Outline platelets.
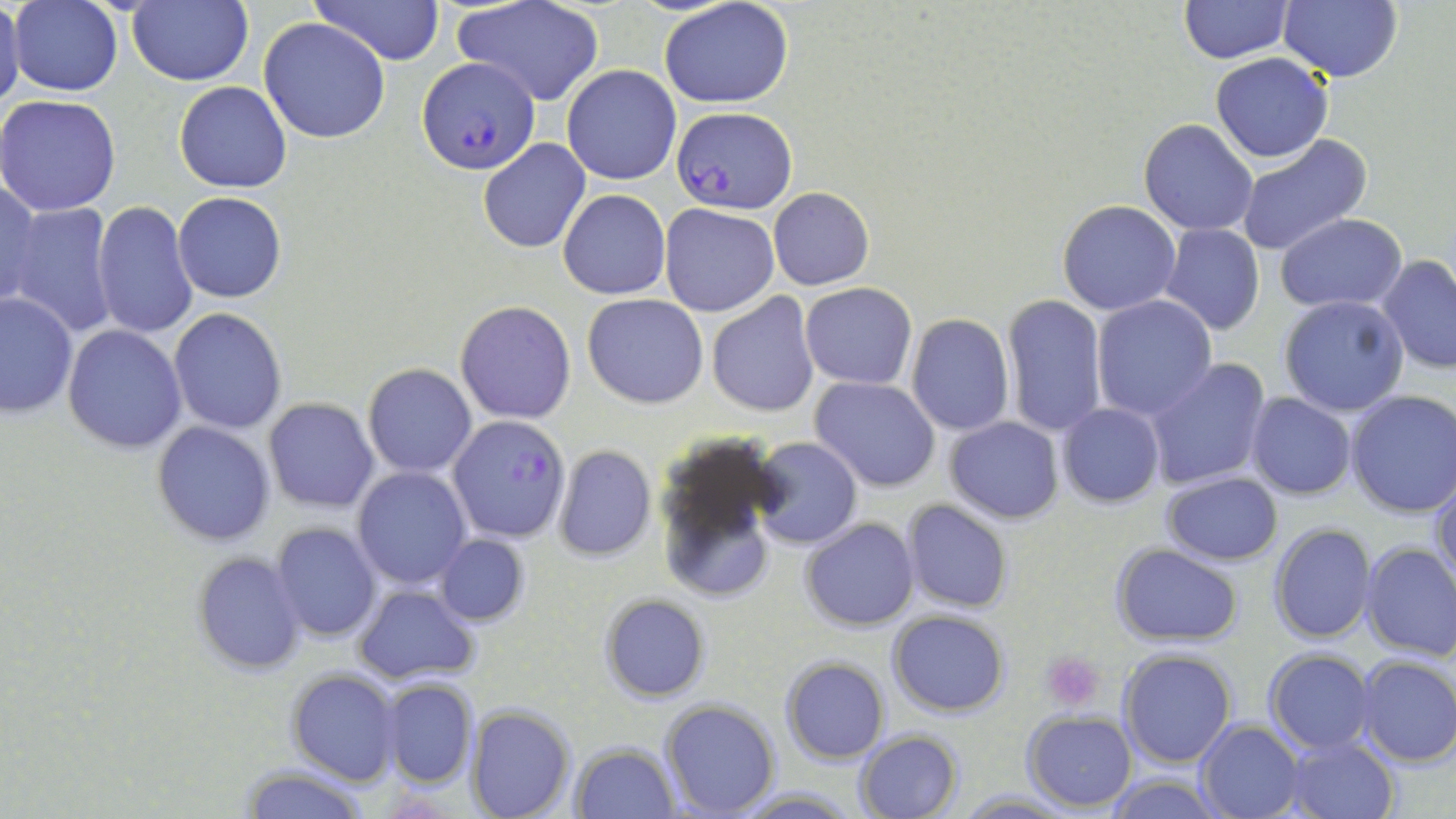

Approximate bounding boxes as (x1,y1)-(x2,y2) corner pairs in pixels.
Platelets: (1042,651)-(1105,711).

Summary:
  - Uninfected red blood cell locations (subset): (0,0)-(25,115), (128,0)-(254,85), (315,0)-(446,64), (660,0)-(796,108), (1178,0)-(1293,62), (1278,0)-(1402,82), (9,1)-(124,98), (455,1)-(604,106), (258,17)-(391,144), (1209,53)-(1333,162), (562,65)-(681,185), (172,80)-(293,193), (0,94)-(122,216), (1138,119)-(1259,236), (1235,136)-(1373,258), (478,138)-(590,252), (1,174)-(41,306), (768,187)-(875,291), (559,189)-(671,299), (172,191)-(287,303), (90,199)-(197,341), (1057,199)-(1180,315), (4,202)-(119,338), (660,203)-(780,317), (1274,213)-(1407,310), (1158,224)-(1266,335), (1378,254)-(1456,374), (799,283)-(917,389), (1,291)-(77,419), (707,291)-(820,418), (583,293)-(710,408), (1000,293)-(1107,437), (1276,294)-(1410,419), (1092,296)-(1218,422), (456,301)-(577,425), (168,308)-(288,433), (905,313)-(1015,436), (64,325)-(186,453), (1144,357)-(1273,491), (362,364)-(477,478), (810,376)-(940,492), (1345,390)-(1455,518), (1246,393)-(1357,499), (263,397)-(379,514), (1057,402)-(1164,507), (944,416)-(1065,523), (152,420)-(276,547), (653,430)-(786,603), (751,437)-(862,550), (553,445)-(656,562), (353,466)-(470,589), (1432,470)-(1456,592), (1160,471)-(1283,565), (901,499)-(1013,614), (802,518)-(919,630), (270,522)-(380,642), (1269,523)-(1376,643), (436,534)-(529,625), (1359,540)-(1456,662), (1110,543)-(1242,646), (191,552)-(307,676), (355,584)-(477,685), (599,593)-(711,702), (888,609)-(1010,717), (1117,648)-(1237,768), (1264,648)-(1377,753), (1353,654)-(1456,768), (781,658)-(889,764), (286,671)-(399,786), (380,678)-(478,788), (660,698)-(781,818), (468,705)-(577,819), (1022,711)-(1136,812), (1195,719)-(1305,818), (855,729)-(962,818), (1281,735)-(1399,818), (570,742)-(680,818), (238,764)-(371,819), (1106,772)-(1221,818), (729,786)-(859,817), (955,790)-(1076,818)
  - Plasmodium falciparum-infected red blood cell locations (subset): (672,106)-(796,213), (448,415)-(571,542)
  - Slide-level diagnosis: Plasmodium falciparum
  - Stain: May-Grünwald-Giemsa
  - Field of view: single
  - Magnification: 1000x
  - Preparation: thin blood film
  - Modality: optical microscopy
  - Image size: 1456×819 pixels